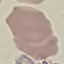
result: negative for malaria parasites
capture: smartphone camera at the microscope eyepiece
stain: Giemsa
image_type: automatically extracted cell patch, resized to 64 × 64 pixels
preparation: thin blood smear